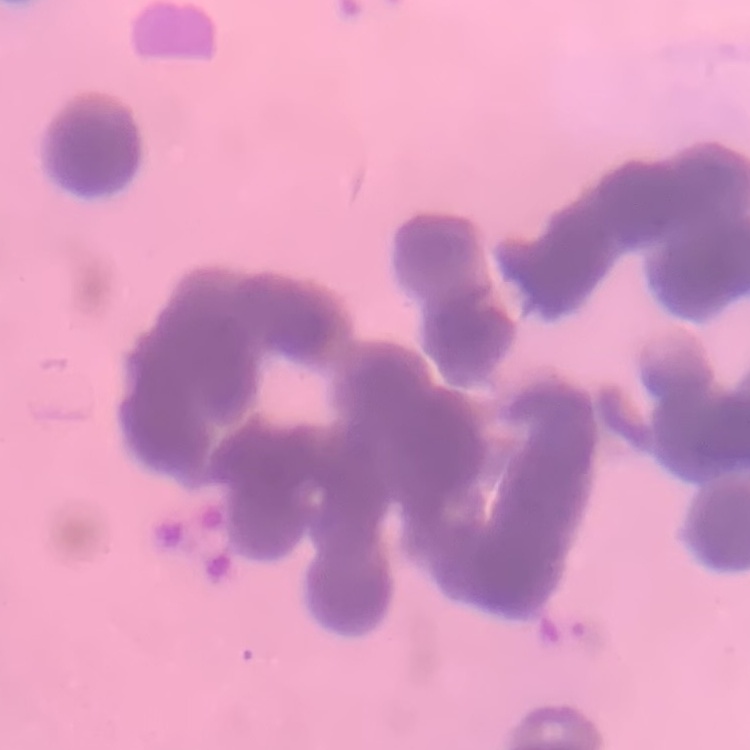

red blood cell morphology = rouleaux formation
stain = Field's or Giemsa
image type = square crop of a larger photomicrograph
preparation = thin peripheral smear